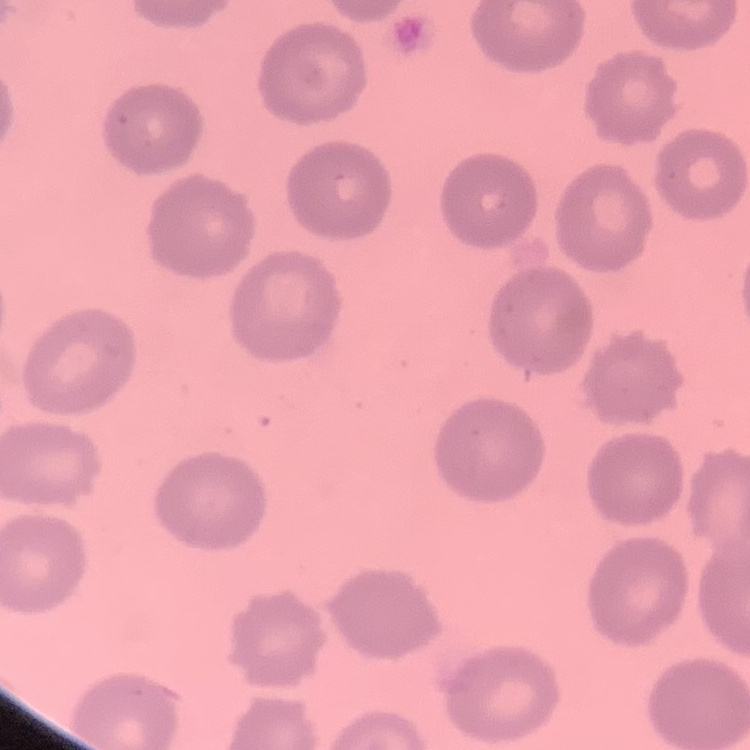
Summary:
  - Erythrocyte morphology: no rouleaux formation
  - Stain: Field's or Giemsa
  - Preparation: thin blood smear
  - Image type: square crop of a larger photomicrograph